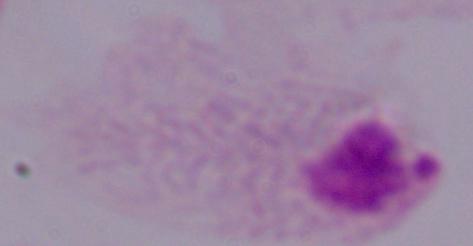 Captured at 1000x magnification. Photomicrograph. A trichomonad is seen.